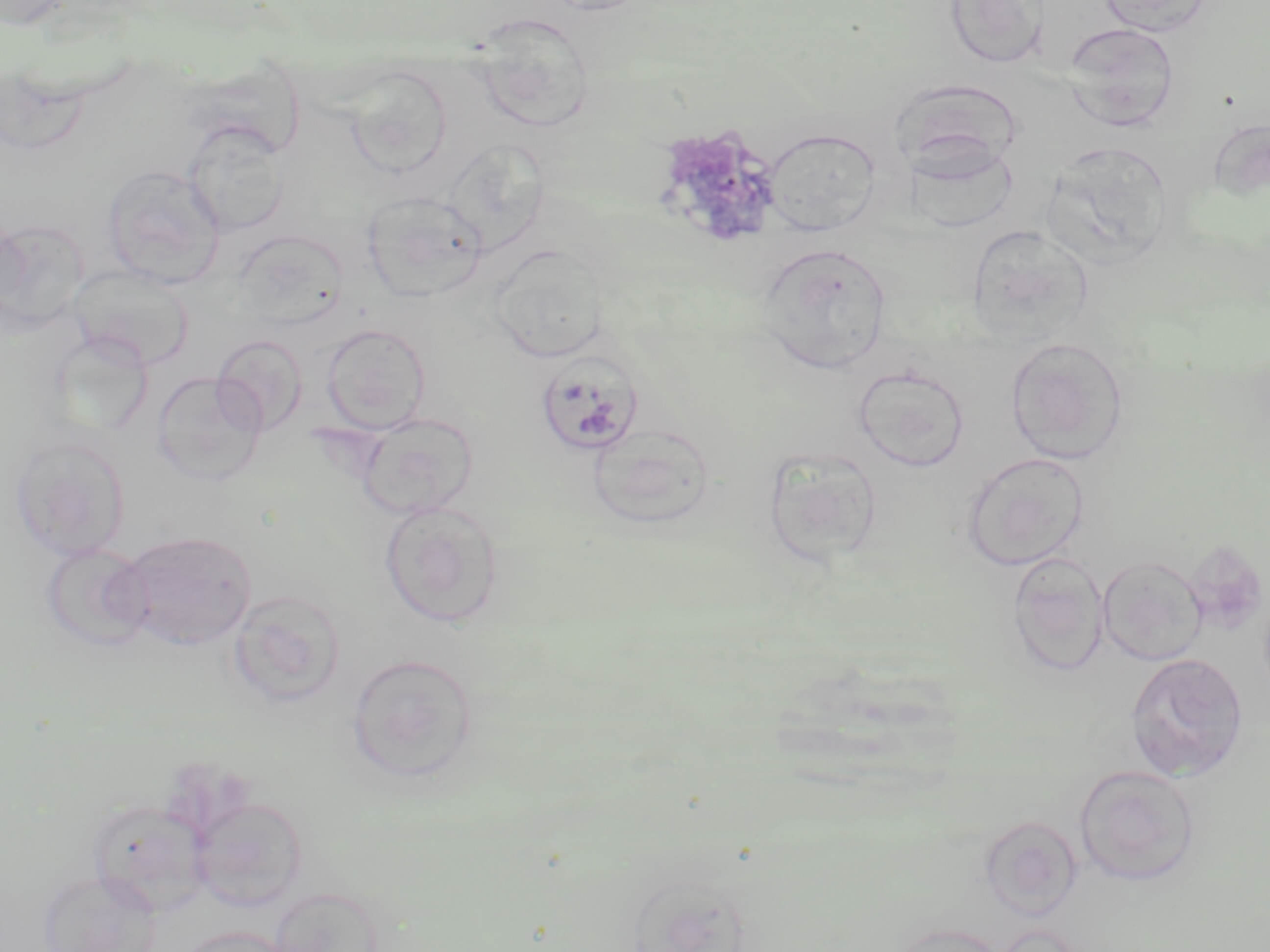
Summary:
  - Coordinate format: approximate bounding boxes as named x1/y1/x2/y2 corners in pixels
  - Plasmodium malariae-infected red blood cell locations: (x1=533, y1=351, x2=646, y2=458)
  - Uninfected red blood cell locations: (x1=0, y1=0, x2=78, y2=30), (x1=532, y1=0, x2=657, y2=15), (x1=943, y1=0, x2=1050, y2=69), (x1=1096, y1=0, x2=1212, y2=36), (x1=471, y1=11, x2=595, y2=132), (x1=1063, y1=23, x2=1180, y2=131), (x1=343, y1=65, x2=453, y2=179), (x1=1208, y1=119, x2=1270, y2=201), (x1=182, y1=121, x2=289, y2=237), (x1=761, y1=127, x2=883, y2=235), (x1=904, y1=140, x2=1020, y2=233), (x1=1041, y1=140, x2=1175, y2=268), (x1=102, y1=164, x2=225, y2=289), (x1=361, y1=190, x2=487, y2=303), (x1=0, y1=219, x2=88, y2=333), (x1=965, y1=224, x2=1094, y2=347), (x1=232, y1=230, x2=349, y2=330), (x1=756, y1=242, x2=893, y2=375), (x1=489, y1=245, x2=610, y2=364), (x1=68, y1=264, x2=194, y2=370), (x1=321, y1=322, x2=430, y2=434), (x1=212, y1=334, x2=308, y2=435), (x1=1004, y1=336, x2=1129, y2=465), (x1=853, y1=364, x2=970, y2=472), (x1=152, y1=371, x2=266, y2=487), (x1=356, y1=411, x2=479, y2=519), (x1=586, y1=421, x2=717, y2=529), (x1=10, y1=432, x2=131, y2=562), (x1=761, y1=446, x2=884, y2=567), (x1=960, y1=452, x2=1090, y2=572), (x1=379, y1=501, x2=505, y2=627), (x1=118, y1=531, x2=257, y2=650), (x1=40, y1=542, x2=153, y2=652), (x1=1006, y1=551, x2=1109, y2=676), (x1=1098, y1=554, x2=1208, y2=666), (x1=227, y1=589, x2=347, y2=709), (x1=1125, y1=652, x2=1249, y2=781), (x1=346, y1=653, x2=480, y2=785), (x1=1074, y1=764, x2=1200, y2=886), (x1=190, y1=794, x2=308, y2=911), (x1=88, y1=798, x2=212, y2=916), (x1=978, y1=815, x2=1082, y2=922), (x1=37, y1=869, x2=161, y2=952), (x1=267, y1=884, x2=386, y2=952), (x1=887, y1=922, x2=1011, y2=952), (x1=174, y1=925, x2=293, y2=952)
  - Slide-level diagnosis: Plasmodium malariae
  - Stain: May-Grünwald-Giemsa
  - Image size: 1270×952 pixels
  - Magnification: 1000x
  - Field of view: single
  - Modality: light microscopy
  - Preparation: thin blood film